Name the blood parasite species.
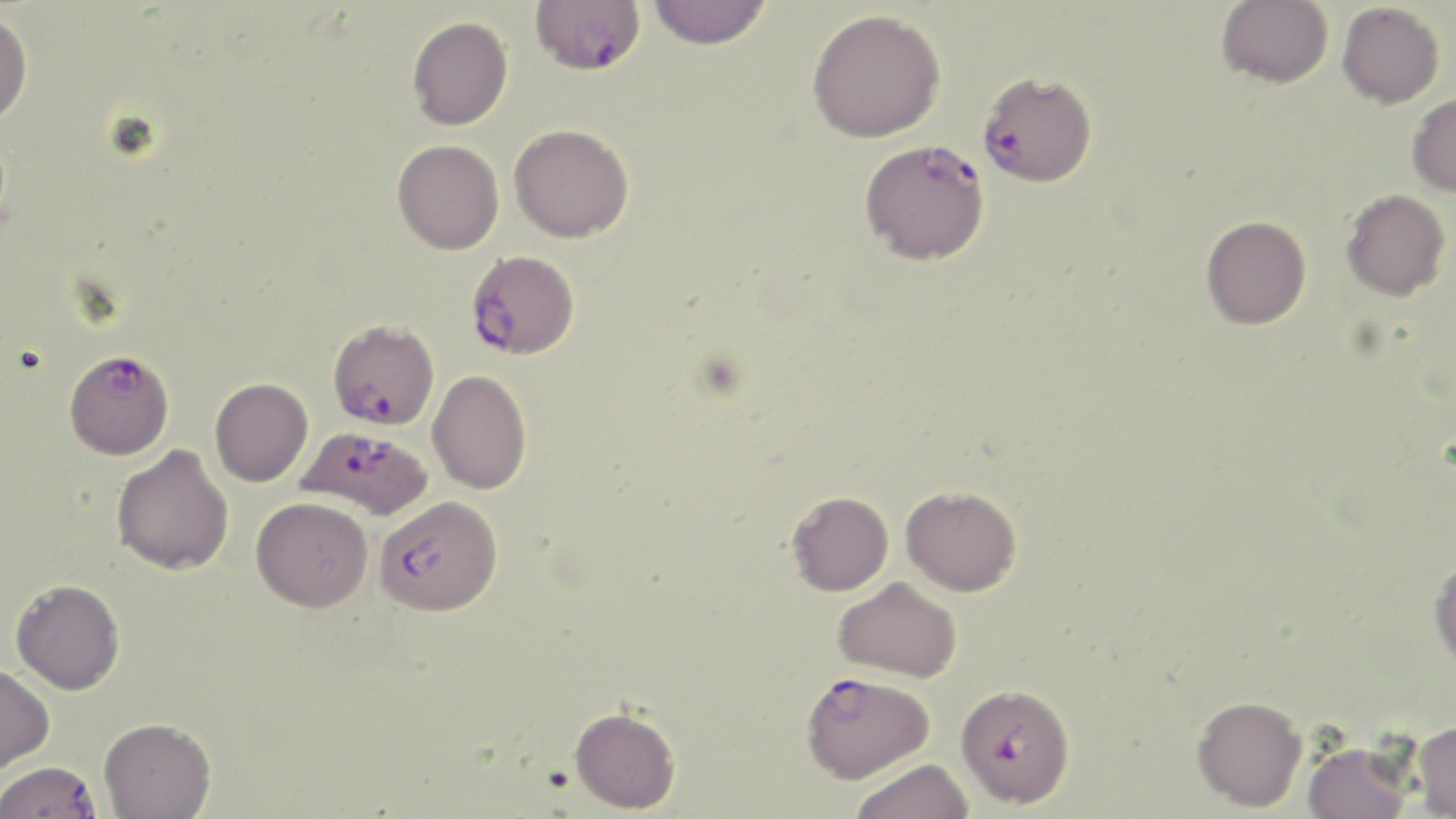

Plasmodium falciparum.

Summary:
  - Coordinate format: approximate bounding boxes as (x1,y1)-(x2,y2) corner pairs in pixels
  - Plasmodium falciparum-infected red blood cell locations: (536,3)-(651,78), (978,69)-(1097,186), (859,138)-(990,265), (466,249)-(580,360), (328,318)-(439,430), (67,351)-(170,463), (298,426)-(433,521), (374,495)-(503,616), (800,670)-(934,783), (956,682)-(1075,807), (0,761)-(101,819)
  - Uninfected red blood cell locations: (647,0)-(773,49), (1216,0)-(1333,88), (1337,2)-(1445,108), (807,8)-(946,142), (0,11)-(33,128), (407,15)-(513,130), (1407,93)-(1456,196), (509,124)-(634,242), (392,139)-(504,254), (1341,189)-(1450,300), (1200,215)-(1311,329), (427,369)-(532,494), (210,378)-(313,486), (111,445)-(234,576), (901,485)-(1022,596), (787,491)-(893,596), (251,497)-(374,612), (1428,555)-(1456,672), (833,576)-(963,682), (11,579)-(125,695), (0,664)-(54,773), (1192,695)-(1307,811), (569,706)-(681,813), (99,717)-(216,818), (1412,720)-(1456,818), (1302,739)-(1412,819), (850,758)-(975,819)
  - Magnification: 1000x
  - Field of view: single
  - Stain: May-Grünwald-Giemsa
  - Modality: light microscopy
  - Image size: 1456×819 pixels
  - Preparation: thin blood film